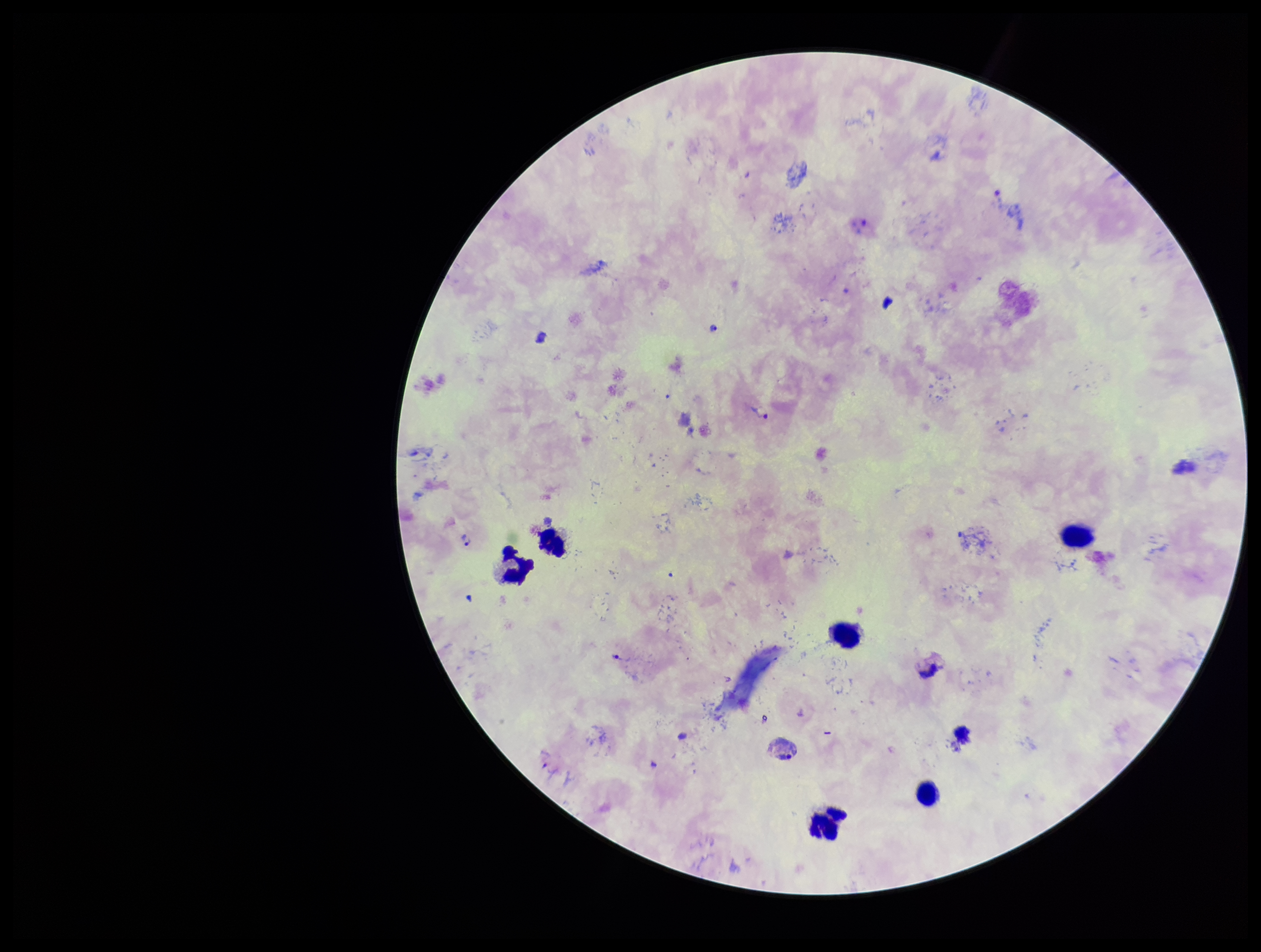

Summary:
  - Capture: smartphone photograph through the microscope eyepiece
  - Image size: 1261×952 pixels
  - Field of view: single
  - Species reported for this patient: Plasmodium vivax
  - Stain: Giemsa
  - Parasite count: 5
  - Preparation: thick
  - Patient malaria status: infected
  - Leukocyte count: 7
  - Plasmodium parasites: detected